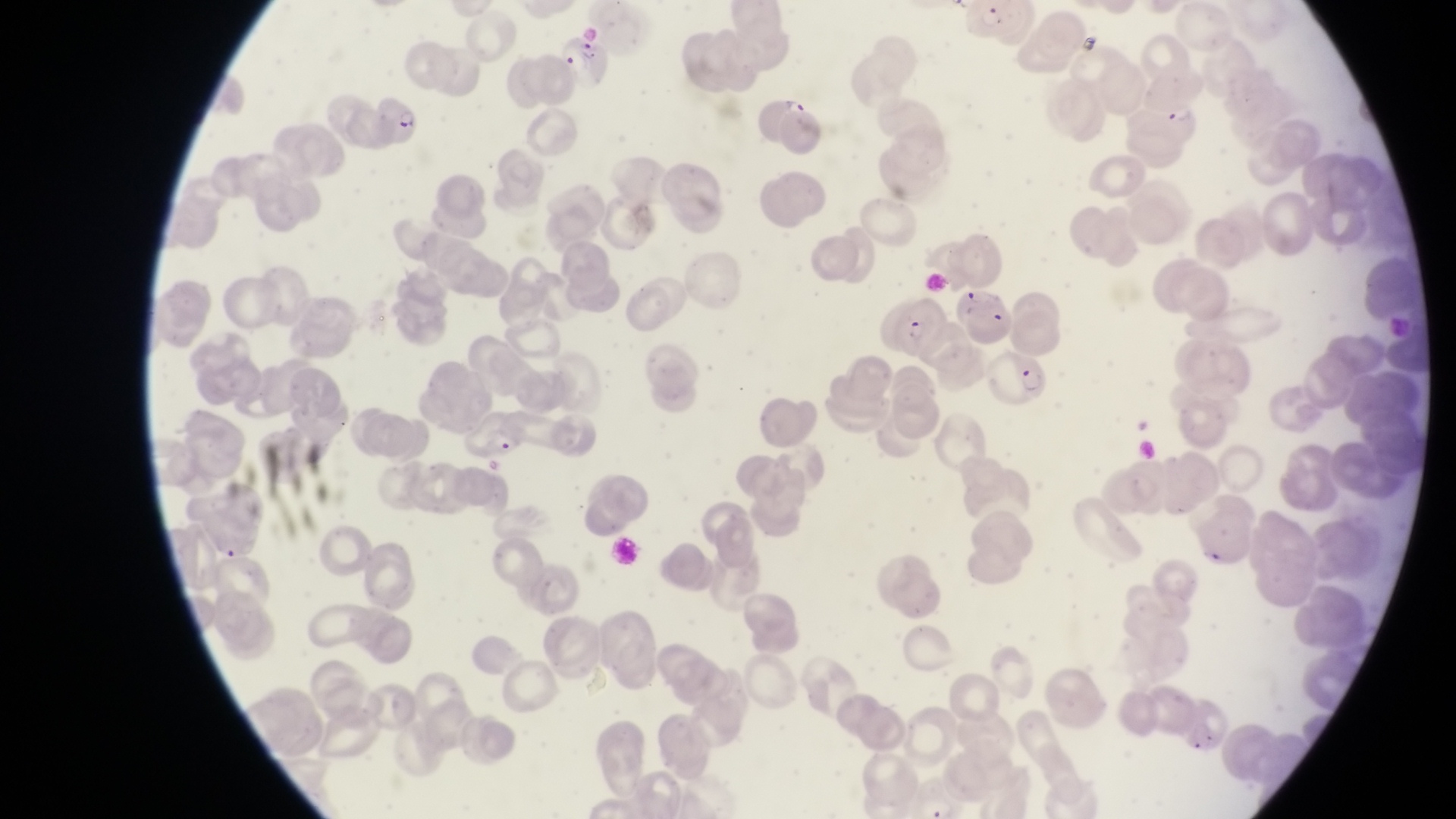

Approximate bounding boxes as {left, top, right, bottom} in pixels.
Summary:
  - Artifact (platelet-like body, stain precipitate, or debris) locations: {1189, 538, 1229, 577}
  - Trophozoite locations: {783, 95, 806, 119}
  - Parasitised red blood cell locations: {561, 35, 613, 77}, {375, 96, 427, 146}, {1142, 98, 1203, 148}, {891, 294, 947, 352}, {987, 353, 1054, 411}
  - Capture: smartphone photograph through the eyepiece of an Olympus CX-23 microscope
  - Field of view: single
  - Country: Uganda
  - Preparation: thin blood film
  - Image size: 1456×819 pixels
  - Magnification: 1000x